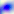

identification = Toxoplasma gondii
magnification = 400x
modality = micrograph